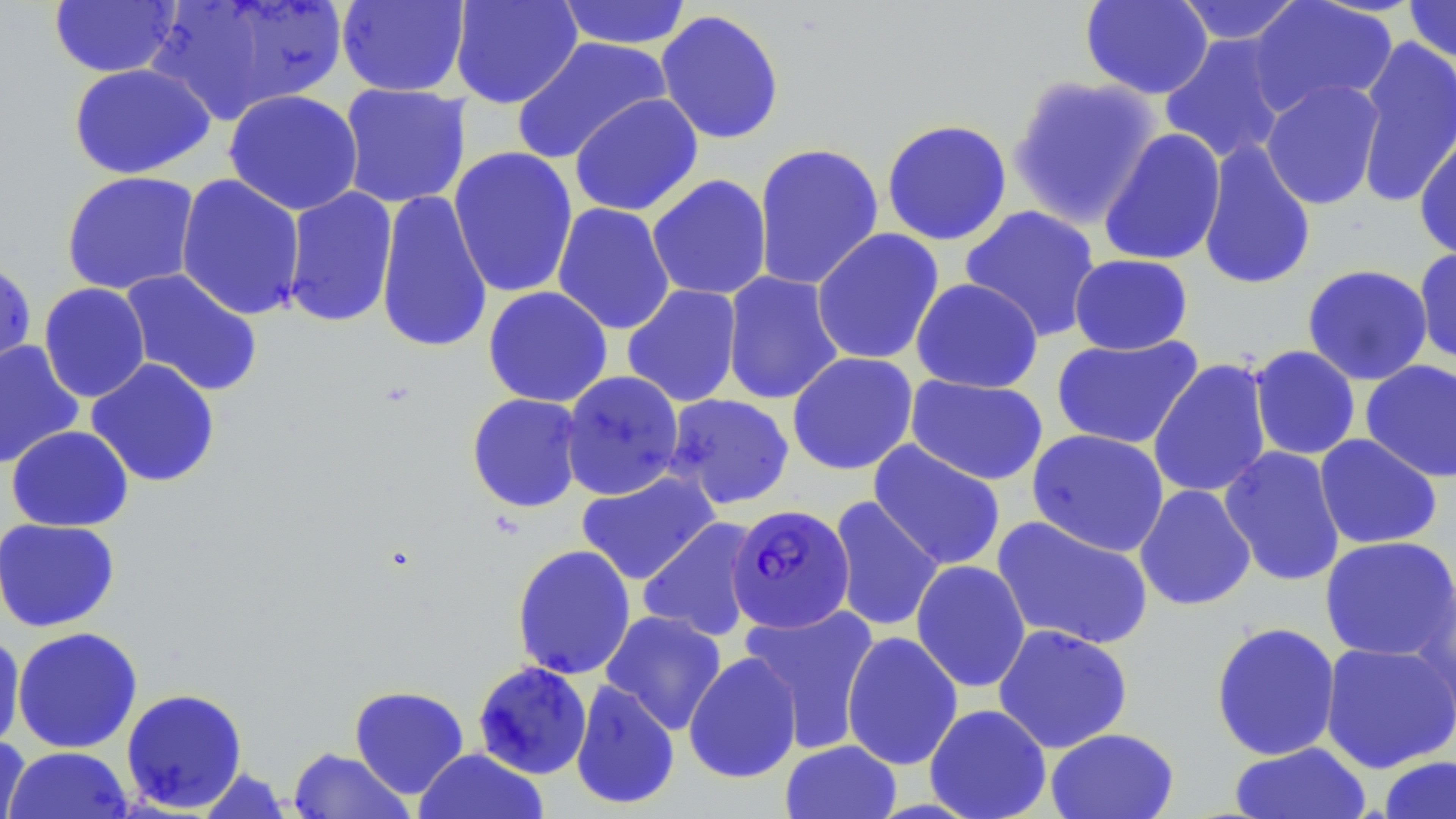

slide-level diagnosis = Plasmodium falciparum
field of view = one of a larger specimen
preparation = thin blood film
stain = May-Grünwald-Giemsa
modality = optical microscopy
uninfected red blood cell locations = approximate bounding boxes as named x1/y1/x2/y2 corners in pixels: (x1=149, y1=0, x2=347, y2=124), (x1=449, y1=0, x2=583, y2=109), (x1=555, y1=0, x2=693, y2=50), (x1=1079, y1=0, x2=1214, y2=99), (x1=1173, y1=0, x2=1308, y2=45), (x1=1248, y1=0, x2=1398, y2=118), (x1=1403, y1=0, x2=1456, y2=64), (x1=48, y1=1, x2=182, y2=77), (x1=336, y1=1, x2=470, y2=97), (x1=655, y1=9, x2=785, y2=145), (x1=1159, y1=34, x2=1289, y2=165), (x1=1354, y1=35, x2=1456, y2=208), (x1=511, y1=36, x2=673, y2=165), (x1=68, y1=63, x2=216, y2=180), (x1=1007, y1=74, x2=1163, y2=230), (x1=1261, y1=79, x2=1385, y2=210), (x1=337, y1=83, x2=471, y2=209), (x1=223, y1=89, x2=364, y2=216), (x1=569, y1=93, x2=703, y2=217), (x1=881, y1=119, x2=1013, y2=246), (x1=1414, y1=125, x2=1456, y2=262), (x1=1098, y1=127, x2=1226, y2=266), (x1=1197, y1=139, x2=1317, y2=291), (x1=752, y1=142, x2=884, y2=291), (x1=448, y1=146, x2=579, y2=298), (x1=60, y1=170, x2=201, y2=295), (x1=175, y1=173, x2=306, y2=321), (x1=646, y1=174, x2=772, y2=300), (x1=281, y1=187, x2=399, y2=328), (x1=375, y1=188, x2=493, y2=355), (x1=551, y1=202, x2=676, y2=335), (x1=959, y1=205, x2=1101, y2=342), (x1=810, y1=228, x2=944, y2=365), (x1=1413, y1=246, x2=1456, y2=365), (x1=1068, y1=253, x2=1193, y2=355), (x1=0, y1=257, x2=37, y2=382), (x1=1302, y1=264, x2=1433, y2=386), (x1=118, y1=268, x2=264, y2=398), (x1=721, y1=271, x2=845, y2=406), (x1=910, y1=278, x2=1044, y2=393), (x1=38, y1=282, x2=151, y2=403), (x1=622, y1=284, x2=743, y2=408), (x1=483, y1=286, x2=613, y2=407), (x1=1051, y1=335, x2=1204, y2=449), (x1=0, y1=340, x2=84, y2=470), (x1=1248, y1=345, x2=1361, y2=460), (x1=786, y1=352, x2=919, y2=475), (x1=86, y1=358, x2=221, y2=488), (x1=1148, y1=358, x2=1273, y2=499), (x1=1360, y1=359, x2=1456, y2=483), (x1=559, y1=370, x2=685, y2=501), (x1=905, y1=375, x2=1049, y2=485), (x1=466, y1=393, x2=584, y2=512), (x1=663, y1=393, x2=795, y2=510), (x1=6, y1=425, x2=133, y2=531), (x1=1027, y1=429, x2=1170, y2=557), (x1=1314, y1=433, x2=1443, y2=550), (x1=868, y1=440, x2=1006, y2=571), (x1=1219, y1=445, x2=1346, y2=587), (x1=576, y1=470, x2=720, y2=585), (x1=1134, y1=484, x2=1256, y2=611), (x1=827, y1=496, x2=945, y2=632), (x1=991, y1=516, x2=1155, y2=651), (x1=0, y1=517, x2=121, y2=633), (x1=637, y1=517, x2=762, y2=642), (x1=1319, y1=535, x2=1456, y2=661), (x1=512, y1=544, x2=636, y2=680), (x1=910, y1=559, x2=1031, y2=693), (x1=1410, y1=574, x2=1456, y2=726), (x1=739, y1=603, x2=880, y2=752), (x1=600, y1=610, x2=727, y2=735), (x1=1210, y1=620, x2=1341, y2=761), (x1=992, y1=624, x2=1133, y2=754), (x1=12, y1=626, x2=143, y2=754), (x1=841, y1=631, x2=963, y2=770), (x1=0, y1=632, x2=25, y2=753), (x1=1320, y1=641, x2=1456, y2=773), (x1=683, y1=651, x2=802, y2=784), (x1=472, y1=661, x2=593, y2=779), (x1=570, y1=679, x2=680, y2=810), (x1=349, y1=685, x2=469, y2=798), (x1=121, y1=687, x2=248, y2=814), (x1=924, y1=703, x2=1052, y2=819), (x1=1045, y1=727, x2=1179, y2=819), (x1=0, y1=734, x2=31, y2=819), (x1=780, y1=739, x2=902, y2=819), (x1=1229, y1=741, x2=1372, y2=819), (x1=3, y1=746, x2=134, y2=819), (x1=287, y1=747, x2=415, y2=819), (x1=413, y1=747, x2=549, y2=819), (x1=1378, y1=755, x2=1456, y2=818), (x1=197, y1=767, x2=292, y2=818)
image size = 1456×819 pixels
magnification = 1000x
Plasmodium falciparum-infected red blood cell locations = approximate bounding boxes as named x1/y1/x2/y2 corners in pixels: (x1=727, y1=503, x2=855, y2=633)